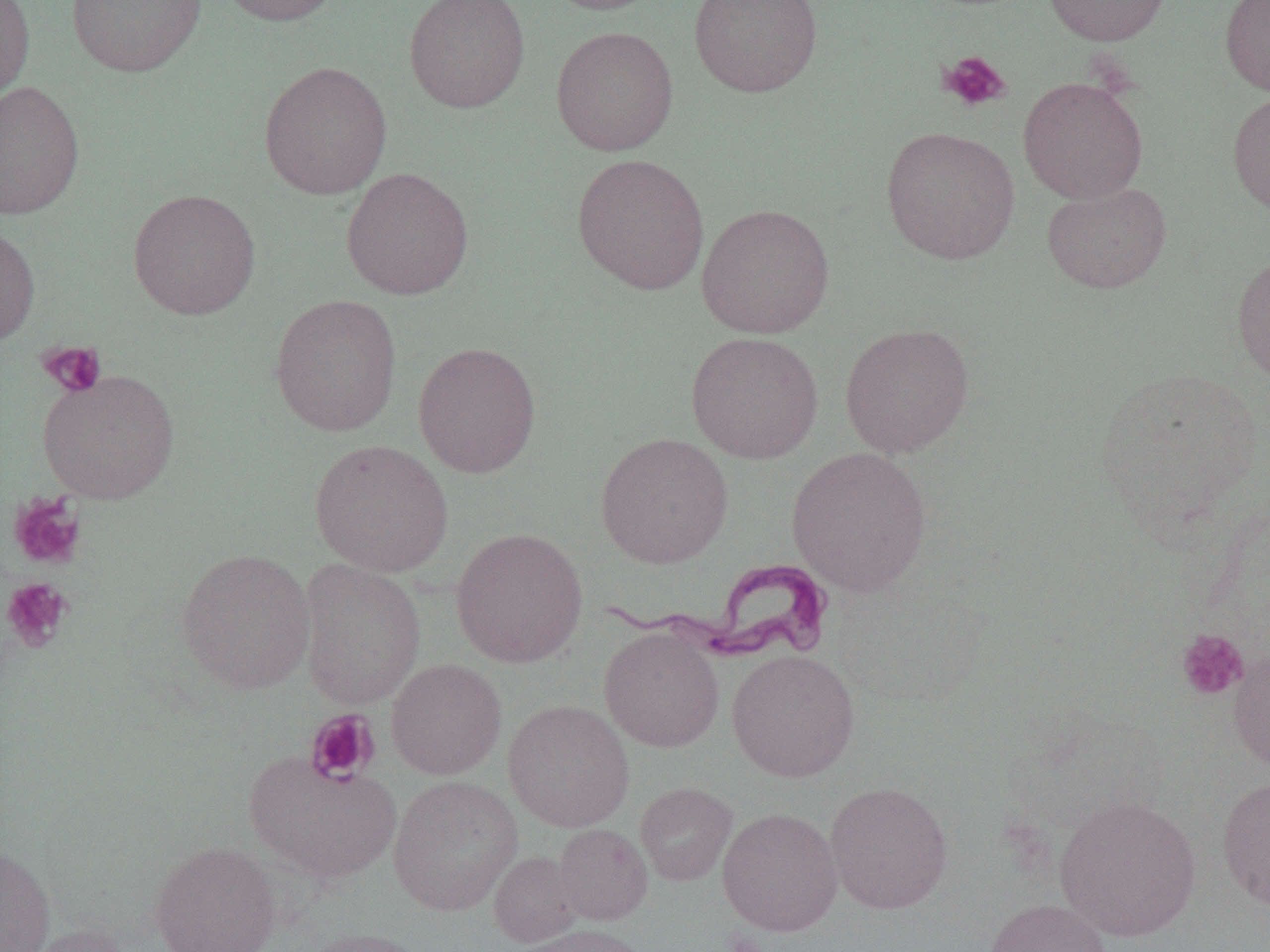
Summary:
  - Coordinate format: approximate bounding boxes as (x1, y1, x2, y2) in pixels
  - Platelet locations: (939, 50, 1013, 112), (37, 341, 107, 398), (9, 493, 88, 572), (0, 577, 74, 653), (1175, 628, 1249, 700), (304, 708, 380, 785), (722, 929, 768, 952)
  - Trypanosoma brucei locations: (590, 560, 836, 664)
  - Uninfected red blood cell locations: (0, 0, 35, 108), (66, 0, 206, 78), (216, 0, 342, 27), (404, 0, 530, 113), (540, 0, 669, 16), (689, 0, 823, 97), (1042, 0, 1172, 46), (1220, 0, 1270, 97), (551, 25, 679, 156), (259, 61, 392, 200), (1018, 76, 1148, 204), (0, 80, 84, 219), (1227, 89, 1270, 217), (880, 126, 1020, 265), (571, 152, 710, 295), (341, 167, 474, 301), (1042, 182, 1172, 293), (128, 188, 261, 321), (696, 203, 835, 339), (0, 225, 40, 349), (1231, 250, 1270, 387), (269, 294, 403, 437), (839, 323, 975, 458), (685, 331, 824, 464), (412, 341, 542, 478), (1093, 367, 1266, 533), (37, 369, 180, 504), (595, 432, 733, 568), (310, 439, 453, 576), (786, 444, 933, 597), (451, 527, 588, 668), (176, 548, 316, 694), (297, 559, 426, 709), (599, 627, 724, 752), (1228, 645, 1270, 773), (727, 649, 860, 782), (386, 658, 507, 779), (503, 699, 635, 832), (244, 751, 401, 884), (388, 775, 522, 916), (1217, 776, 1270, 912), (824, 780, 953, 914), (635, 782, 737, 886), (1053, 794, 1202, 941), (717, 807, 843, 935), (553, 823, 653, 925), (149, 841, 281, 952), (0, 843, 55, 952), (489, 851, 584, 947), (984, 898, 1113, 952), (17, 921, 133, 952), (515, 923, 649, 952), (301, 927, 435, 952)
  - Slide-level diagnosis: Trypanosoma brucei
  - Modality: optical microscopy
  - Image size: 1270×952 pixels
  - Magnification: 1000x
  - Field of view: single
  - Preparation: thin blood smear